Identify the parasite.
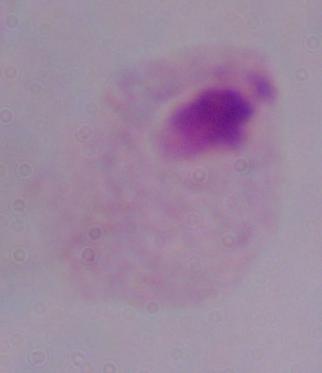

A trichomonad.

1000x magnification. Photomicrograph.